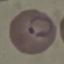
malaria status = parasitized
capture = smartphone camera at the microscope eyepiece
stain = Giemsa
image type = automatically extracted cell patch, resized to 64 × 64 pixels
preparation = thin smear